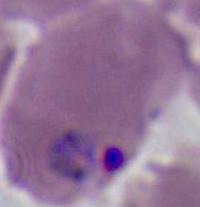

Summary:
  - Modality: photomicrograph
  - Magnification: 400x or 1000x
  - Identification: Plasmodium